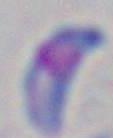

Summary:
  - Magnification: 1000x
  - Modality: photomicrograph
  - Identification: Toxoplasma gondii